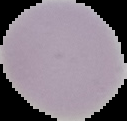
Summary:
  - Image type: cell region segmented out of the field of view; surrounding area masked to black
  - Preparation: thin blood film
  - Malaria status: uninfected
  - Image size: 127×121 pixels